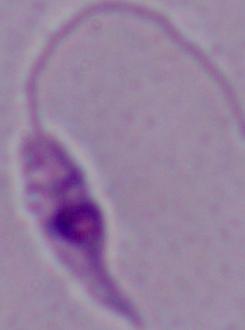

Summary:
  - Identification: Leishmania
  - Magnification: 1000x
  - Modality: photomicrograph